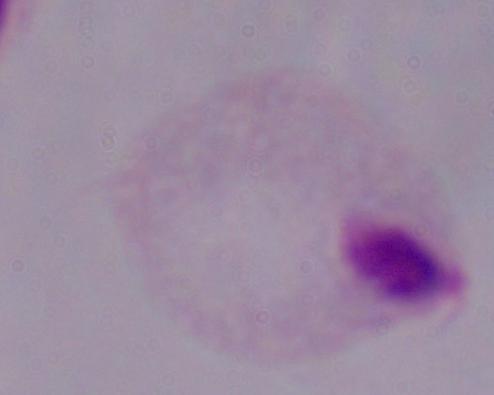

A trichomonad is seen. Micrograph. 1000x magnification.